Locate every Plasmodium parasite and every leukocyte.
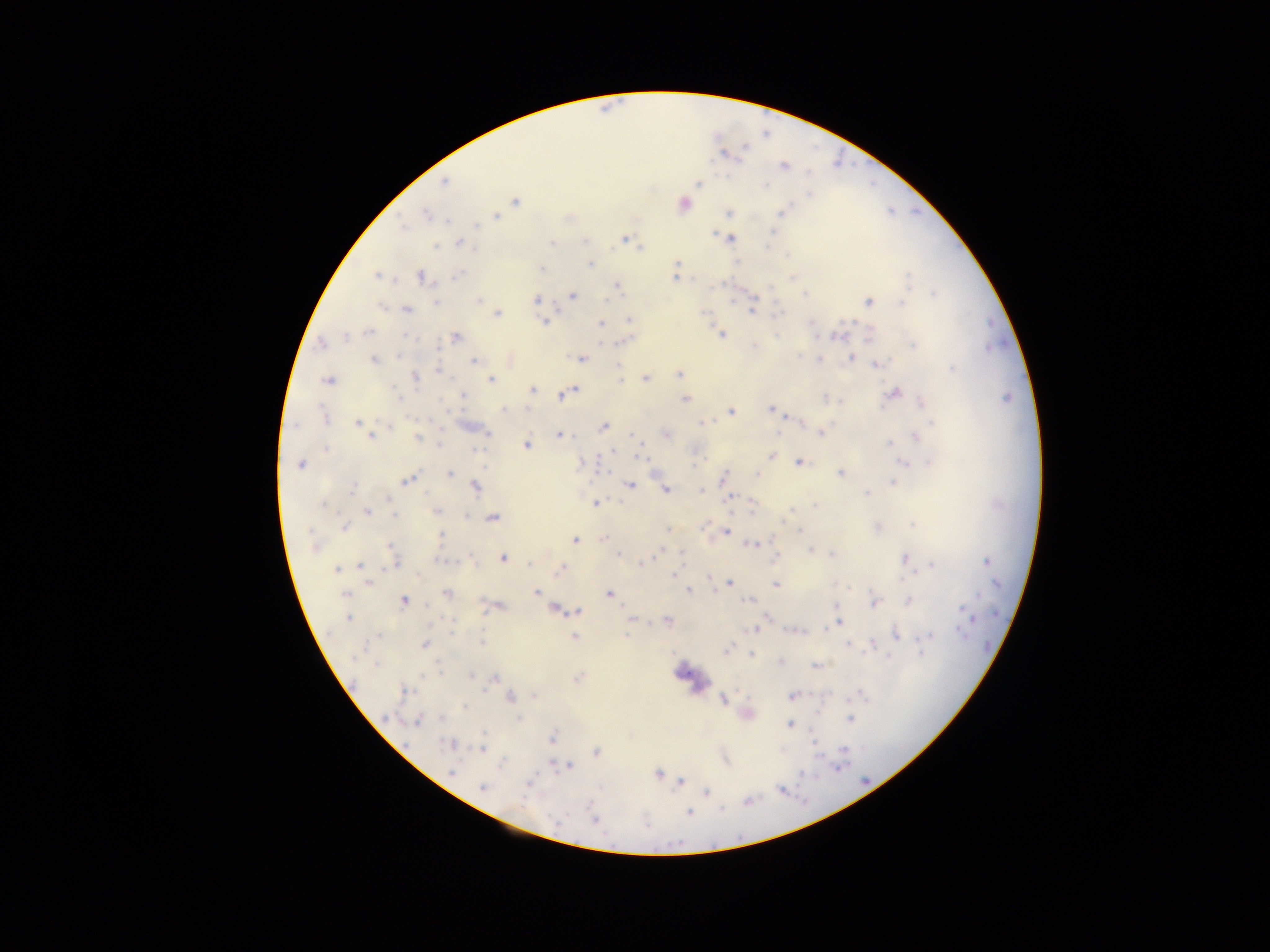

Approximate centers as (x, y) in pixels.
Plasmodium parasites: (766, 133), (724, 152), (783, 166), (444, 181), (697, 185), (765, 187), (514, 202), (686, 204), (729, 212), (781, 213), (426, 215), (494, 216), (447, 221), (404, 225), (475, 226), (773, 229), (713, 234), (624, 237), (733, 238), (583, 241), (458, 242), (550, 242), (435, 247), (765, 247), (640, 249), (786, 256), (677, 264), (592, 266), (675, 273), (458, 274), (419, 275), (375, 276), (910, 277), (793, 279), (616, 286), (932, 292), (804, 294), (574, 296), (608, 296), (477, 299), (535, 299), (900, 301), (869, 302), (436, 303), (382, 306), (406, 309), (777, 312), (498, 313), (752, 313), (630, 320), (544, 321), (600, 323), (368, 330), (723, 334), (456, 337), (836, 337), (342, 339), (868, 339), (623, 342), (913, 344), (754, 345), (985, 348), (400, 355), (797, 355), (851, 358), (582, 359), (372, 360), (821, 360), (473, 361), (877, 364), (952, 368), (619, 371), (439, 372), (679, 374), (645, 377), (415, 378), (621, 379), (491, 380), (325, 381), (531, 390), (573, 391), (895, 392), (560, 396), (462, 397), (1005, 398), (685, 399), (827, 399), (923, 400), (769, 408), (503, 409), (732, 411), (778, 413), (322, 415), (357, 422), (932, 423), (701, 424), (604, 425), (487, 432), (820, 433), (666, 434), (777, 434), (633, 435), (441, 436), (560, 436), (372, 437), (417, 438), (917, 438), (891, 442), (440, 444), (527, 446), (478, 450), (613, 450), (771, 455), (640, 457), (904, 461), (798, 462), (928, 462), (300, 464), (693, 464), (449, 472), (756, 472), (841, 473), (724, 477), (405, 482), (892, 483), (630, 485), (474, 487), (353, 488), (701, 489), (666, 490), (866, 494), (731, 496), (595, 503), (602, 503), (814, 505), (322, 507), (432, 510), (437, 512), (368, 513), (394, 516), (782, 518), (785, 518), (493, 519), (912, 524), (705, 525), (344, 529), (667, 530), (726, 530), (799, 530), (441, 534), (728, 534), (604, 538), (575, 541), (770, 541), (754, 544), (749, 545), (391, 546), (314, 548), (811, 551), (832, 552), (617, 553), (681, 553), (657, 557), (775, 558), (908, 558), (503, 559), (987, 562), (528, 563), (396, 564), (932, 565), (360, 566), (638, 566), (391, 567), (559, 568), (336, 569), (673, 573), (368, 583), (729, 583), (775, 583), (846, 588), (687, 590), (535, 593), (608, 593), (346, 595), (403, 600), (745, 600), (908, 601), (875, 603), (961, 607), (553, 610), (487, 612), (566, 612), (577, 613), (348, 618), (630, 618), (767, 618), (667, 620), (975, 621), (633, 623), (838, 624), (754, 629), (785, 631), (451, 632), (628, 632), (896, 634), (960, 634), (930, 635), (575, 636), (376, 638), (482, 641), (845, 643), (424, 645), (848, 646), (725, 651), (867, 651), (751, 653), (921, 654), (888, 658), (377, 664), (814, 664), (473, 676), (495, 677), (486, 693), (536, 695), (790, 697), (511, 698), (724, 701), (465, 707), (438, 718), (519, 718), (848, 721), (417, 722), (789, 725), (484, 733), (552, 737), (814, 742), (453, 744), (484, 745), (847, 749), (482, 751), (595, 752), (501, 764), (840, 764), (569, 765), (836, 767), (451, 772), (659, 774), (802, 774), (680, 781), (481, 788), (706, 791), (720, 808), (689, 812), (557, 819), (595, 821).
No leukocytes observed.

Summary:
  - Field of view: single
  - Capture: mobile-phone photograph through a microscope
  - Country: Ghana
  - Preparation: thick blood film
  - Image size: 1270×952 pixels